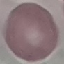
malaria status = uninfected
preparation = thin smear
stain = Giemsa
capture = smartphone camera at the microscope eyepiece
image type = automatically extracted cell patch, resized to 64 × 64 pixels